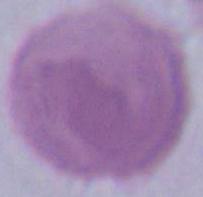

1000x magnification. Micrograph. An erythrocyte is seen.